Describe the morphology of the red blood cells.
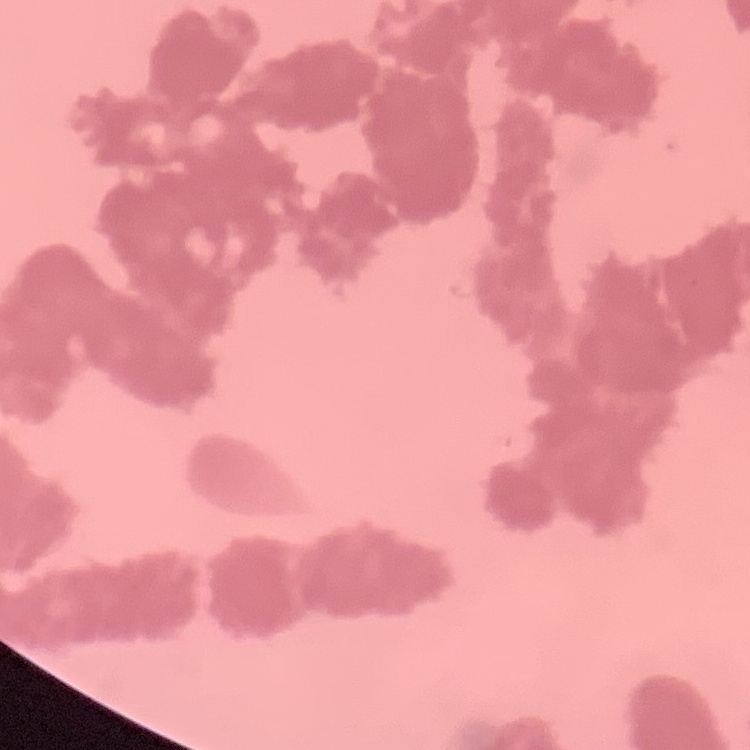

Rouleaux formation.

{
  "stain": "Field's or Giemsa",
  "image_type": "square crop of a larger photomicrograph",
  "preparation": "thin blood film"
}